Identify the blood parasite species.
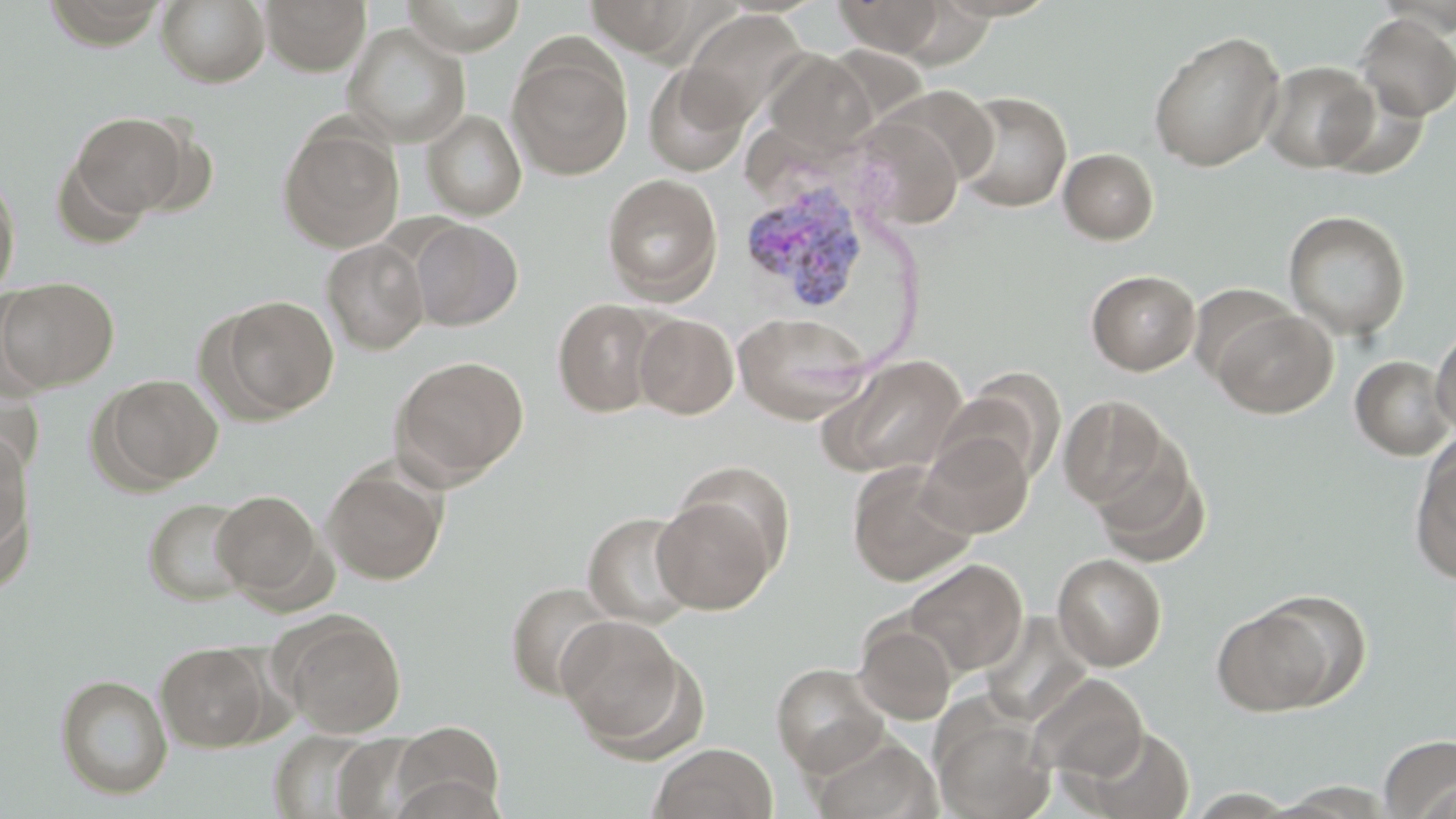
Plasmodium vivax.

modality = light microscopy
magnification = 1000x
uninfected red blood cell locations = approximate bounding boxes as (x1, y1, x2, y2) in pixels: (157, 0, 270, 87), (260, 0, 370, 75), (400, 0, 528, 55), (584, 0, 704, 58), (834, 0, 947, 56), (1356, 12, 1456, 121), (344, 23, 471, 147), (1148, 30, 1286, 171), (507, 43, 633, 181), (763, 52, 875, 156), (1260, 60, 1379, 173), (643, 64, 750, 177), (954, 91, 1072, 212), (422, 109, 527, 220), (69, 112, 192, 221), (849, 116, 964, 229), (278, 123, 405, 253), (1058, 148, 1159, 244), (0, 171, 20, 299), (602, 173, 723, 303), (1283, 210, 1411, 340), (409, 219, 523, 330), (322, 238, 429, 355), (1086, 269, 1200, 375), (0, 277, 119, 393), (216, 296, 340, 418), (552, 297, 663, 418), (1210, 306, 1338, 418), (733, 312, 871, 424), (634, 313, 739, 419), (1430, 324, 1456, 434), (390, 354, 529, 487), (822, 355, 969, 480), (1349, 355, 1454, 460), (952, 370, 1066, 485), (97, 374, 223, 489), (0, 379, 44, 485), (1058, 395, 1174, 512), (918, 430, 1034, 538), (0, 432, 31, 558), (1087, 438, 1211, 567), (1410, 441, 1456, 583), (847, 462, 976, 586), (322, 464, 447, 585), (211, 489, 326, 603), (651, 492, 780, 615), (143, 497, 253, 605), (582, 510, 700, 628), (1052, 553, 1167, 671), (903, 558, 1027, 676), (506, 581, 617, 700), (1211, 605, 1338, 716), (981, 612, 1094, 726), (280, 614, 407, 738), (557, 616, 688, 749), (854, 618, 958, 725), (155, 641, 270, 751), (771, 662, 889, 776), (55, 674, 173, 799), (1029, 674, 1148, 781), (933, 712, 1054, 819), (389, 720, 505, 816), (1081, 727, 1196, 818), (269, 729, 382, 819), (331, 733, 432, 817), (811, 734, 940, 819), (1379, 734, 1456, 816), (649, 742, 778, 819)
image size = 1456×819 pixels
Plasmodium vivax-infected red blood cell locations = approximate bounding boxes as (x1, y1, x2, y2) in pixels: (740, 178, 872, 314)
stain = May-Grünwald-Giemsa
preparation = thin blood smear
field of view = single